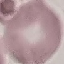

Result: no malaria parasites seen. Cell patch, automatically extracted from a larger field of view and resized to 64 × 64 pixels. Acquired by smartphone through the microscope eyepiece. Giemsa stain. Thin smear of blood.